Outline each uninfected red blood cell.
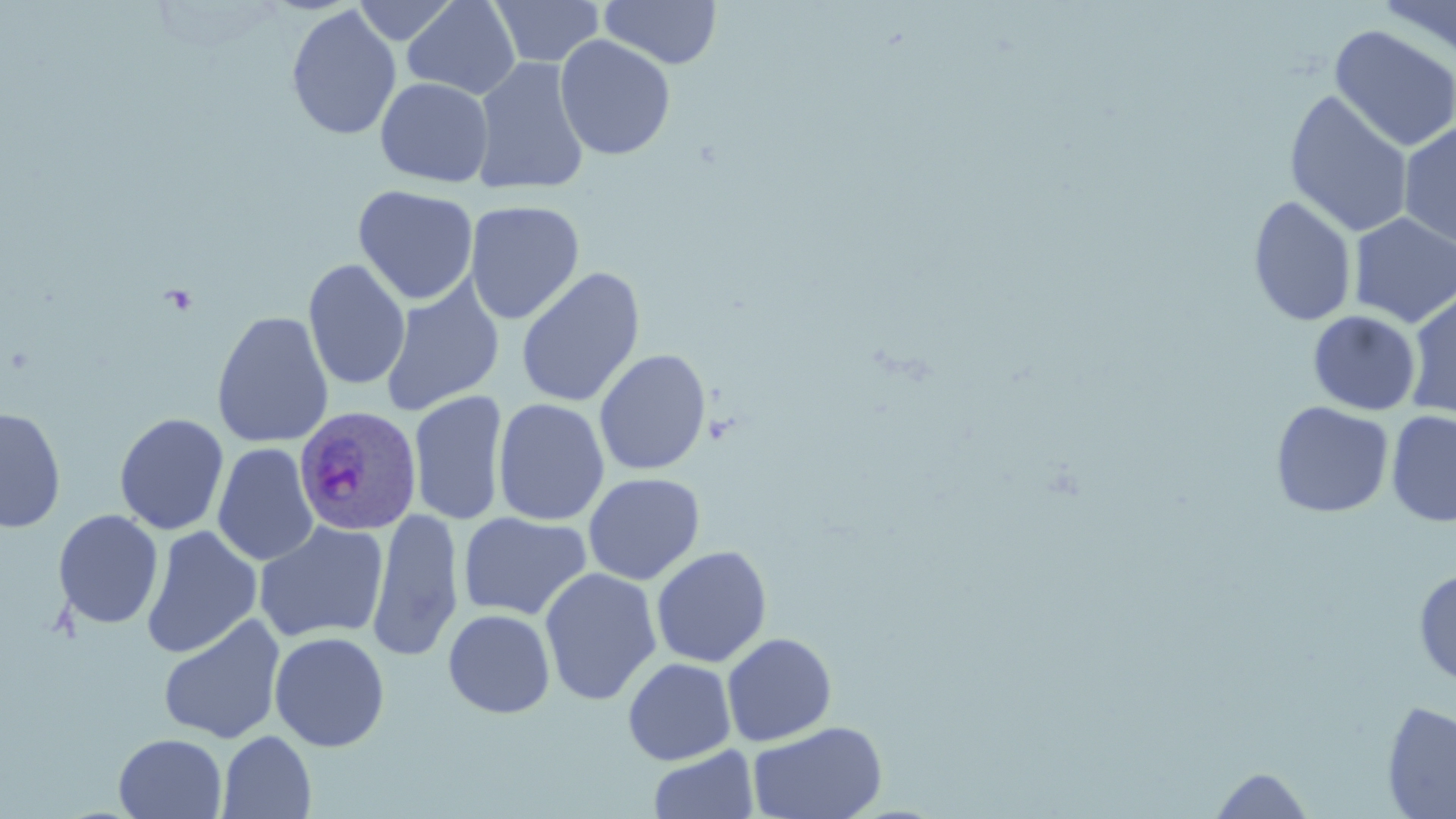
Approximate bounding boxes as (x1, y1, x2, y2) in pixels.
Uninfected red blood cells: (354, 0, 458, 44), (489, 0, 604, 68), (599, 0, 723, 69), (1378, 0, 1456, 66), (402, 1, 520, 100), (286, 5, 402, 141), (1329, 24, 1456, 153), (554, 35, 676, 160), (471, 57, 589, 196), (375, 77, 494, 187), (1283, 91, 1414, 239), (1398, 122, 1456, 250), (353, 185, 478, 305), (1248, 196, 1357, 326), (465, 200, 585, 324), (1348, 212, 1456, 327), (303, 258, 411, 391), (516, 267, 645, 408), (380, 279, 504, 416), (1404, 289, 1456, 421), (1308, 310, 1420, 415), (212, 311, 333, 449), (594, 349, 711, 475), (408, 390, 509, 526), (493, 398, 610, 526), (1270, 401, 1394, 519), (1, 406, 67, 533), (1386, 410, 1456, 526), (113, 413, 229, 536), (212, 443, 319, 567), (582, 472, 705, 585), (366, 507, 465, 663), (52, 509, 163, 629), (458, 511, 592, 621), (253, 521, 389, 644), (141, 525, 262, 659), (650, 545, 773, 668), (539, 567, 662, 706), (1413, 568, 1456, 688), (443, 609, 555, 718), (158, 614, 286, 745), (269, 631, 390, 752), (722, 633, 837, 746), (622, 657, 736, 765), (1381, 700, 1456, 818), (747, 720, 887, 819), (217, 730, 316, 818), (113, 733, 227, 818), (648, 745, 759, 819), (1207, 766, 1318, 818).

{
  "slide_level_diagnosis": "Plasmodium ovale",
  "magnification": "1000x",
  "field_of_view": "one of a larger specimen",
  "plasmodium_ovale_infected_red_blood_cell_locations": "approximate bounding boxes as (x1, y1, x2, y2) in pixels: (294, 405, 422, 535)",
  "image_size": "1456×819 pixels",
  "modality": "optical microscopy",
  "preparation": "thin blood smear",
  "stain": "May-Grünwald-Giemsa"
}